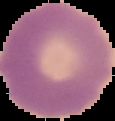

Summary:
  - Malaria status: uninfected
  - Preparation: thin blood film
  - Image type: segmented cell region on a black background
  - Image size: 115×121 pixels